Report the malaria status of this cell.
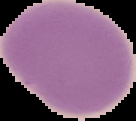
Uninfected.

Summary:
  - Image type: cell region segmented out of the field of view; surrounding area masked to black
  - Preparation: thin blood film
  - Image size: 136×121 pixels